Report the malaria status of this cell.
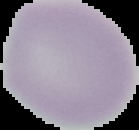
It is uninfected.

Summary:
  - Image type: segmented cell region on a black background
  - Image size: 139×130 pixels
  - Preparation: thin blood film